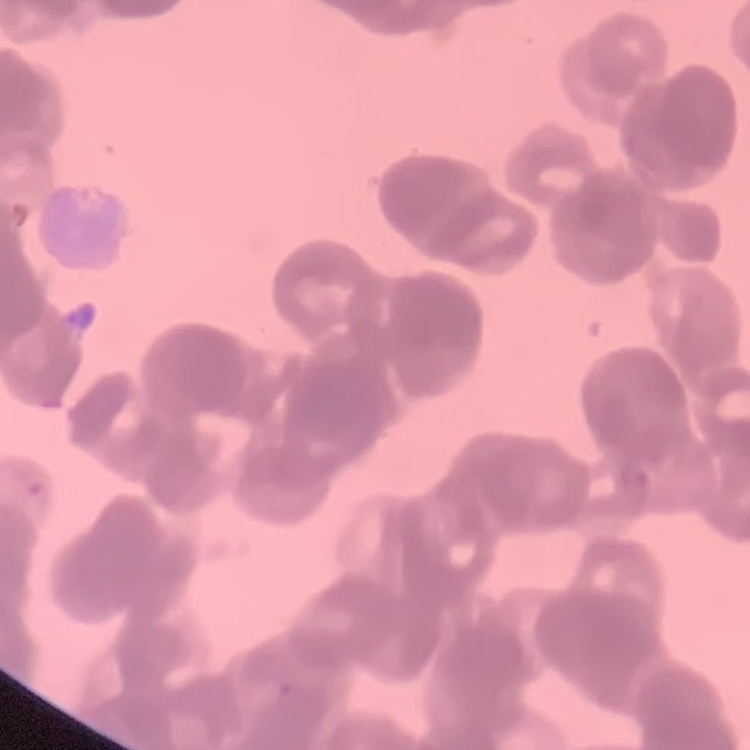
Summary:
  - Red blood cell morphology: rouleaux formation
  - Preparation: thin peripheral smear
  - Stain: Field's or Giemsa
  - Image type: one tile cut from a larger photomicrograph